Assess the morphology of the erythrocytes.
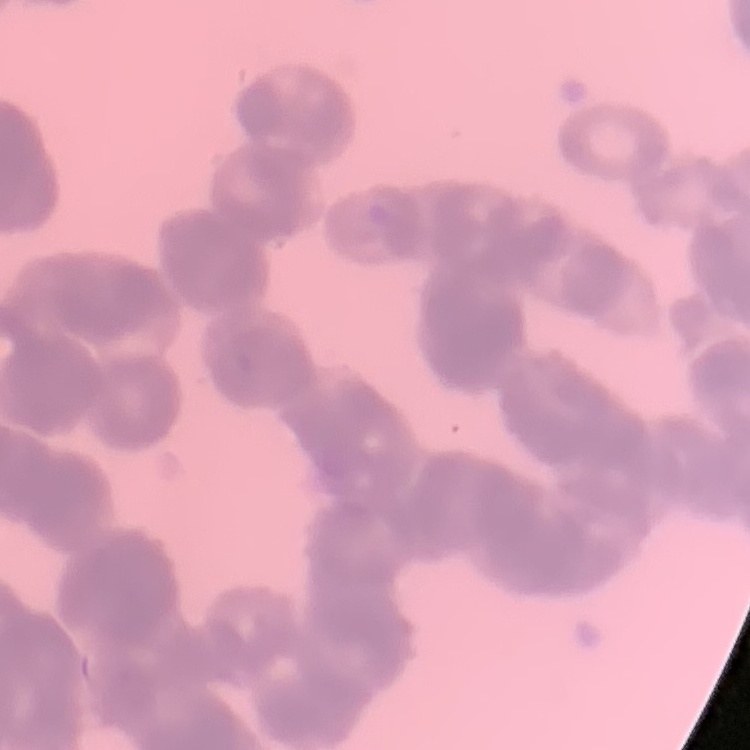
Rouleaux formation.

Thin blood smear. Square crop of a larger photomicrograph. Field's or Giemsa stain.